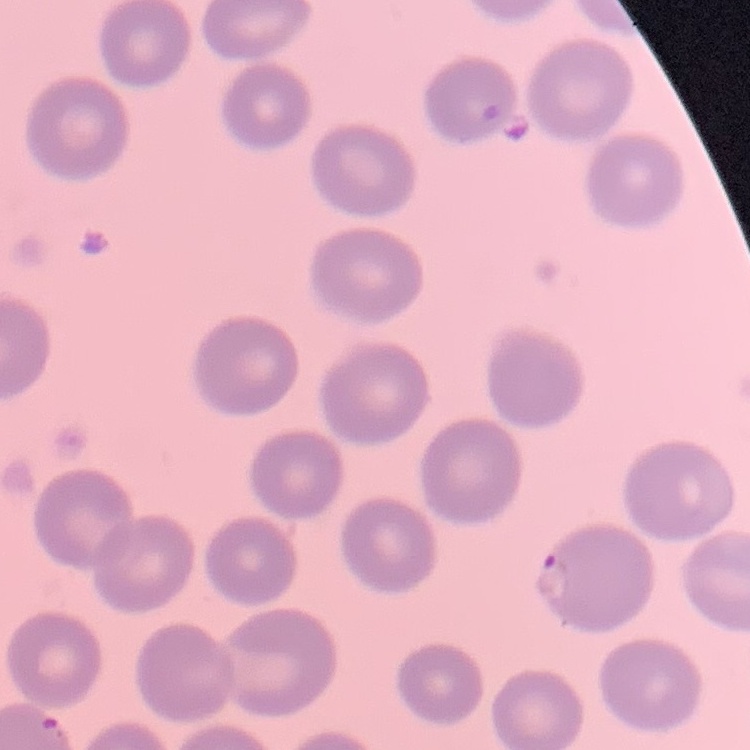

Summary:
  - Erythrocyte morphology: no rouleaux formation
  - Image type: one tile cut from a larger photomicrograph
  - Stain: Field's or Giemsa
  - Preparation: thin peripheral smear